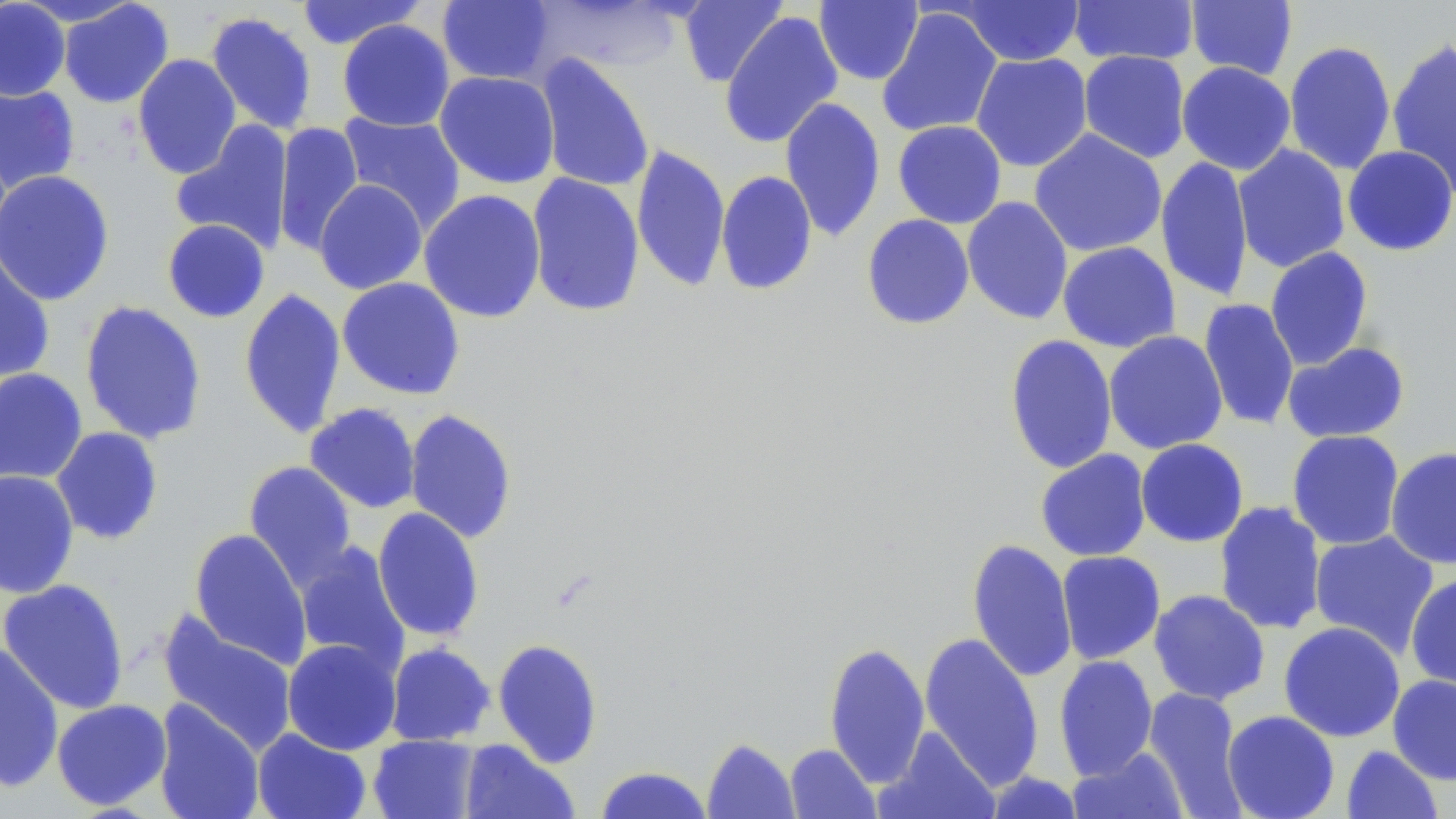

{
  "slide_level_diagnosis": "negative for blood parasites",
  "modality": "light microscopy",
  "magnification": "1000x",
  "stain": "May-Grünwald-Giemsa",
  "field_of_view": "one of a larger specimen",
  "preparation": "thin blood film",
  "image_size": "1456×819 pixels",
  "uninfected_red_blood_cell_locations": "approximate bounding boxes as [x1, y1, x2, y2] in pixels: [295, 0, 425, 50], [437, 0, 557, 85], [678, 0, 788, 87], [814, 0, 923, 85], [0, 1, 71, 101], [16, 1, 142, 27], [58, 1, 174, 108], [531, 1, 690, 75], [954, 1, 1085, 66], [1068, 1, 1199, 66], [1185, 1, 1298, 81], [876, 7, 1002, 138], [719, 11, 842, 149], [205, 12, 318, 135], [337, 20, 454, 132], [1386, 37, 1456, 198], [1284, 41, 1396, 175], [1078, 50, 1191, 163], [970, 52, 1093, 172], [132, 53, 242, 179], [536, 54, 655, 193], [1177, 61, 1296, 175], [435, 71, 560, 189], [0, 82, 80, 194], [779, 96, 885, 243], [338, 112, 465, 231], [170, 120, 294, 254], [893, 120, 1007, 228], [273, 122, 364, 257], [1029, 129, 1167, 257], [631, 144, 730, 292], [1233, 144, 1350, 273], [1342, 145, 1456, 256], [1156, 157, 1254, 302], [0, 170, 116, 306], [715, 170, 818, 296], [526, 173, 645, 317], [314, 179, 427, 295], [419, 189, 546, 323], [961, 196, 1073, 325], [861, 214, 975, 330], [162, 219, 270, 322], [1057, 241, 1181, 353], [1264, 247, 1374, 371], [0, 249, 56, 385], [336, 277, 466, 400], [239, 287, 346, 439], [1198, 298, 1299, 431], [79, 300, 207, 444], [1104, 330, 1228, 454], [1004, 334, 1117, 474], [1281, 340, 1410, 443], [0, 368, 88, 486], [304, 403, 421, 513], [404, 408, 518, 544], [51, 426, 164, 545], [1286, 429, 1405, 550], [1135, 439, 1249, 546], [1386, 446, 1456, 569], [1035, 449, 1151, 561], [242, 460, 357, 587], [0, 470, 80, 598], [1213, 501, 1327, 635], [372, 507, 485, 642], [189, 528, 312, 668], [1309, 531, 1440, 659], [967, 538, 1078, 684], [293, 541, 409, 672], [1056, 550, 1165, 664], [1406, 573, 1456, 691], [0, 579, 130, 714], [1149, 589, 1270, 705], [158, 612, 298, 755], [1278, 621, 1405, 742], [919, 632, 1044, 790], [282, 638, 402, 755], [492, 638, 604, 768], [823, 641, 930, 787], [0, 642, 64, 793], [385, 642, 496, 746], [1053, 655, 1158, 780], [1387, 674, 1456, 785], [1142, 688, 1249, 817], [52, 698, 172, 811], [152, 699, 265, 819], [1222, 710, 1340, 819], [874, 726, 1000, 818], [252, 728, 372, 819], [368, 735, 480, 819], [702, 737, 799, 818], [459, 740, 579, 819], [785, 743, 881, 818], [1341, 745, 1444, 819], [1067, 746, 1190, 819], [594, 766, 713, 818], [982, 771, 1085, 818]"
}